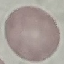
Result: no malaria parasites seen. Thin blood smear. Cell patch, automatically extracted from a larger field of view and resized to 64 × 64 pixels. Giemsa-stained preparation. Acquired by smartphone through the microscope eyepiece.